Classify this cell by malaria status.
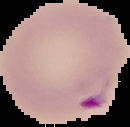

Parasitized.

image size = 130×127 pixels
image type = cell region segmented out of the field of view; surrounding area masked to black
preparation = thin blood film